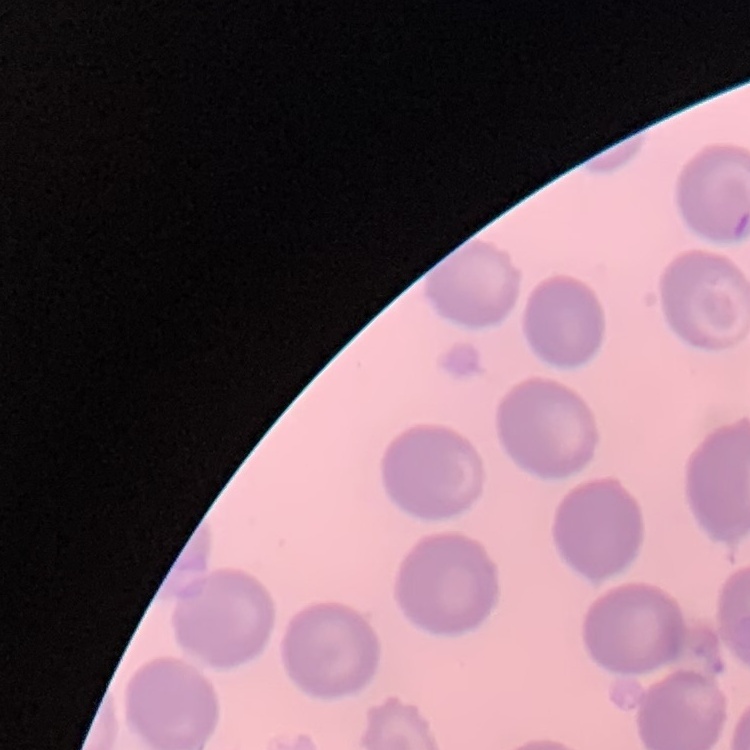

Summary:
  - Red blood cell morphology: no rouleaux formation
  - Stain: Field's or Giemsa
  - Image type: one tile cut from a larger photomicrograph
  - Preparation: thin blood film